State which parasite is depicted.
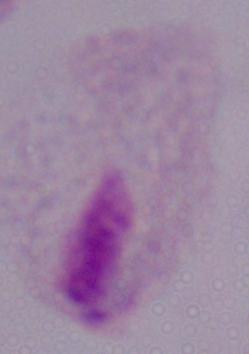
This is a trichomonad.

magnification = 1000x
modality = micrograph